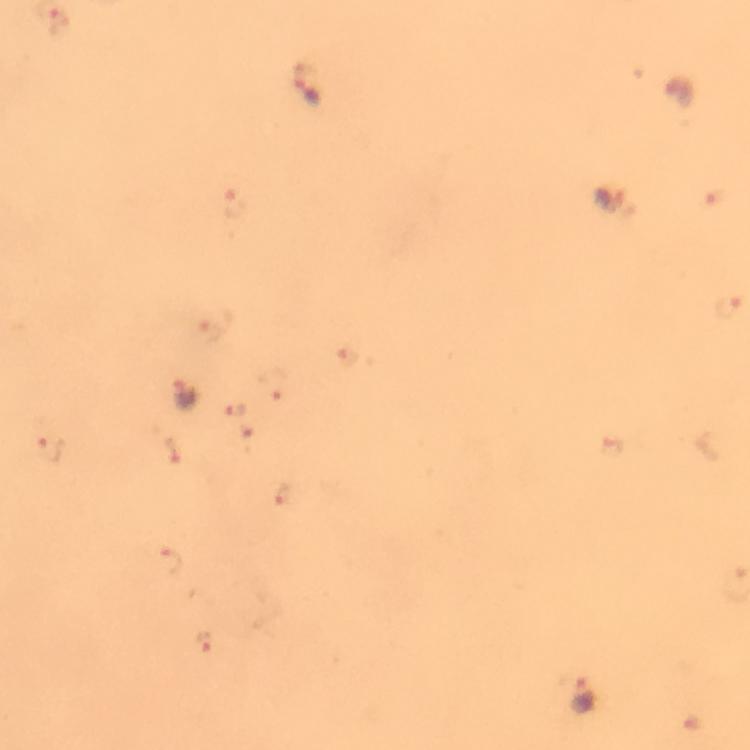 Approximate centers as {x, y} in pixels. Malaria parasite locations: {308, 86}, {233, 201}, {614, 203}, {729, 306}, {185, 395}, {51, 449}, {583, 696}. Cropped region of a single field of view. Thick blood smear. Giemsa-stained preparation. Image is 750×750 pixels. Immersion oil was used. At 100x magnification. From a malaria diagnostic workup. Photographed through the microscope with a smartphone camera.